Comment on the morphology of the erythrocytes.
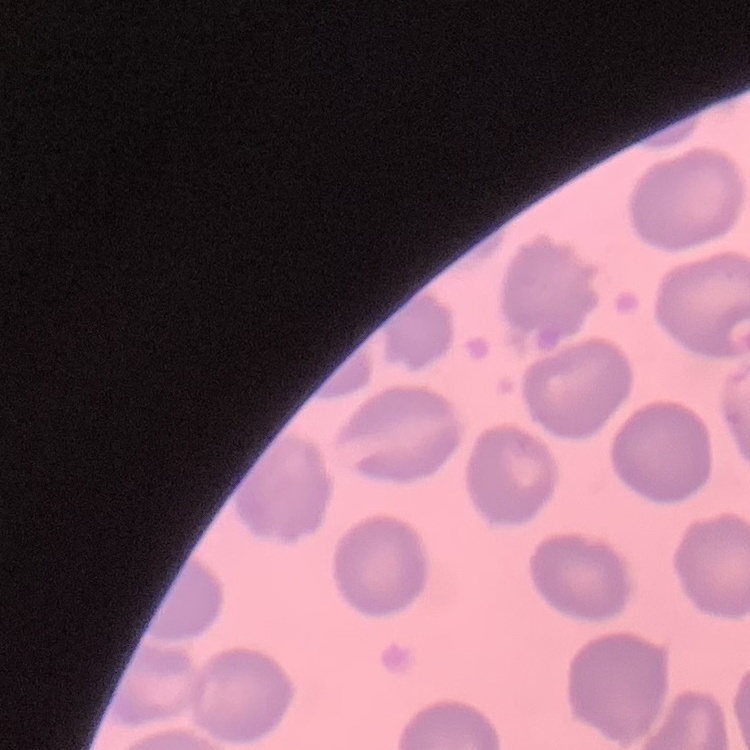

No rouleaux formation.

Summary:
  - Image type: square crop of a larger photomicrograph
  - Preparation: thin peripheral smear
  - Stain: Field's or Giemsa